Classify this cell by malaria status.
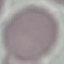
It is uninfected.

preparation = thin smear
capture = smartphone camera at the microscope eyepiece
image type = automatically extracted cell patch, resized to 64 × 64 pixels
stain = Giemsa